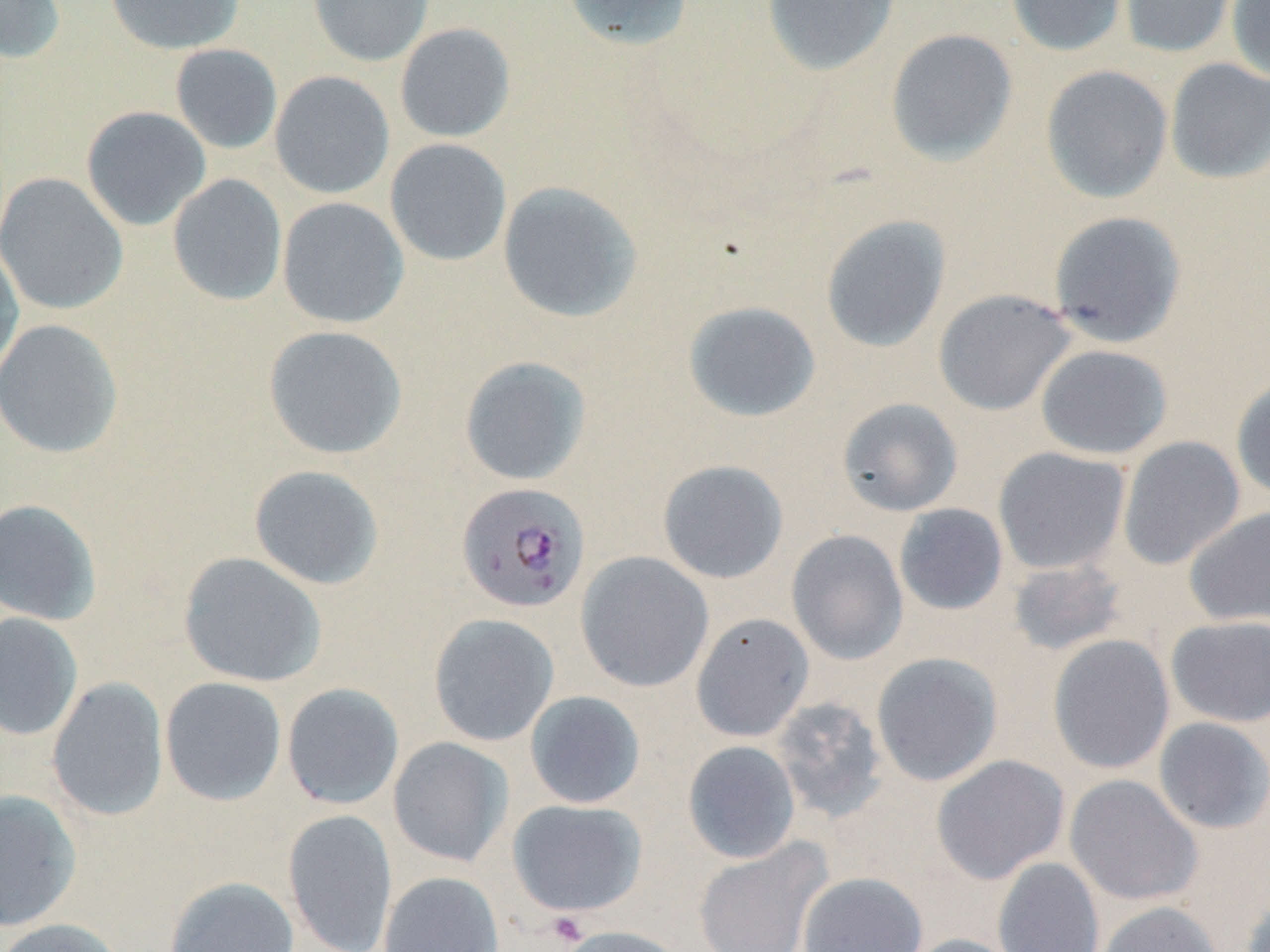
slide_level_diagnosis: Plasmodium falciparum
uninfected_red_blood_cell_locations: 'approximate bounding boxes as (x1,y1)-(x2,y2) corner pairs in pixels: (0,0)-(66,64), (105,0)-(244,55), (308,0)-(434,67), (560,0)-(695,51), (761,0)-(900,77), (1007,0)-(1129,57), (1119,0)-(1238,58), (1226,0)-(1270,83), (394,23)-(516,143), (885,28)-(1018,166), (170,43)-(283,154), (1165,58)-(1270,184), (1040,65)-(1174,203), (269,70)-(395,199), (81,106)-(212,231), (384,138)-(512,267), (0,172)-(129,315), (167,173)-(287,306), (496,180)-(643,323), (277,197)-(409,329), (1048,210)-(1187,348), (821,215)-(952,352), (0,240)-(24,381), (933,289)-(1076,416), (683,300)-(821,423), (0,319)-(123,458), (262,325)-(408,460), (1035,344)-(1174,460), (459,356)-(592,486), (1231,376)-(1270,502), (836,398)-(964,517), (1117,436)-(1246,570), (993,447)-(1130,575), (657,459)-(789,584), (248,464)-(385,590), (0,498)-(102,626), (894,503)-(1009,616), (1184,506)-(1270,627), (786,529)-(908,665), (178,551)-(326,688), (575,551)-(714,693), (1006,558)-(1129,657), (0,613)-(83,742), (428,613)-(560,747), (690,613)-(814,743), (1166,615)-(1270,727), (1048,634)-(1175,775), (871,652)-(1003,787), (46,676)-(169,822), (159,677)-(287,806), (281,683)-(404,810), (524,690)-(646,809), (770,696)-(890,823), (1153,717)-(1270,834), (387,737)-(514,868), (682,740)-(801,864), (931,754)-(1070,884), (1064,774)-(1203,906), (0,790)-(82,932), (507,799)-(648,917), (282,808)-(398,952), (693,838)-(833,952), (993,857)-(1104,952), (379,871)-(505,952), (798,872)-(927,952), (164,875)-(300,952), (1239,888)-(1270,952), (1096,900)-(1224,952), (0,918)-(127,952), (554,925)-(690,952), (901,934)-(1024,952)'
platelet_locations: 'approximate bounding boxes as (x1,y1)-(x2,y2) corner pairs in pixels: (544,912)-(591,948)'
plasmodium_falciparum_infected_red_blood_cell_locations: 'approximate bounding boxes as (x1,y1)-(x2,y2) corner pairs in pixels: (456,482)-(590,613)'
modality: light microscopy
preparation: thin blood smear
stain: May-Grünwald-Giemsa
field_of_view: single
image_size: 1270×952 pixels
magnification: 1000x